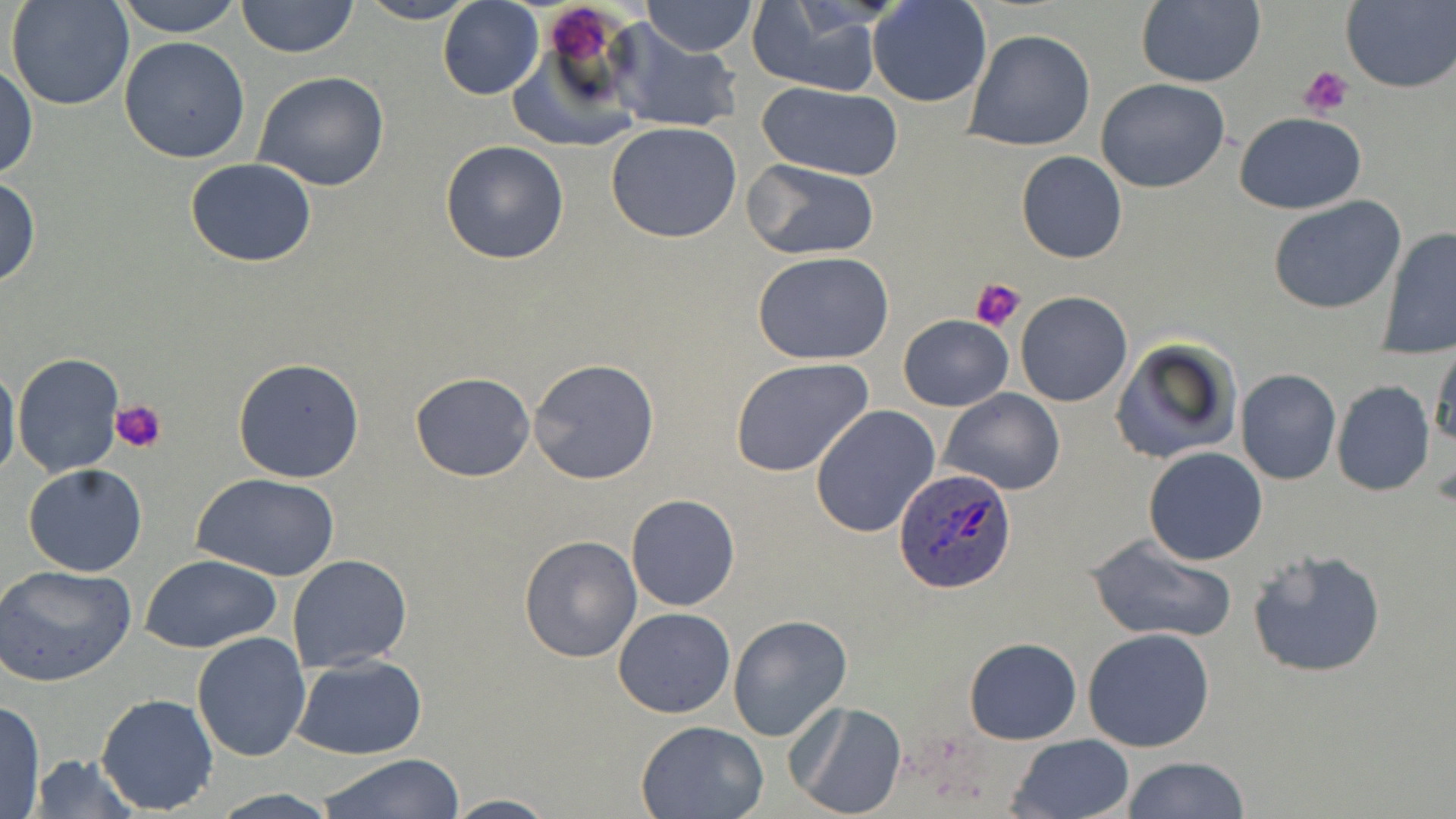
Approximate bounding boxes as named x1/y1/x2/y2 corners in pixels. Platelet locations: (x1=549, y1=8, x2=611, y2=62), (x1=1299, y1=65, x2=1352, y2=118), (x1=972, y1=277, x2=1024, y2=333), (x1=110, y1=398, x2=168, y2=454). Uninfected red blood cell locations: (x1=5, y1=0, x2=134, y2=111), (x1=114, y1=0, x2=244, y2=36), (x1=235, y1=0, x2=359, y2=60), (x1=639, y1=0, x2=758, y2=57), (x1=355, y1=1, x2=479, y2=24), (x1=437, y1=1, x2=544, y2=100), (x1=867, y1=1, x2=993, y2=107), (x1=1133, y1=1, x2=1267, y2=88), (x1=1341, y1=1, x2=1456, y2=93), (x1=743, y1=6, x2=890, y2=95), (x1=608, y1=24, x2=744, y2=134), (x1=506, y1=28, x2=643, y2=151), (x1=964, y1=28, x2=1096, y2=151), (x1=119, y1=37, x2=251, y2=163), (x1=0, y1=64, x2=37, y2=180), (x1=252, y1=71, x2=390, y2=192), (x1=1094, y1=77, x2=1230, y2=194), (x1=756, y1=82, x2=904, y2=182), (x1=1234, y1=112, x2=1367, y2=214), (x1=605, y1=122, x2=743, y2=243), (x1=439, y1=139, x2=570, y2=264), (x1=1016, y1=150, x2=1127, y2=264), (x1=185, y1=158, x2=317, y2=268), (x1=744, y1=160, x2=880, y2=259), (x1=0, y1=176, x2=41, y2=289), (x1=1267, y1=194, x2=1406, y2=315), (x1=1379, y1=229, x2=1456, y2=356), (x1=752, y1=252, x2=896, y2=364), (x1=1014, y1=292, x2=1134, y2=407), (x1=898, y1=315, x2=1013, y2=410), (x1=1109, y1=338, x2=1242, y2=465), (x1=1431, y1=342, x2=1456, y2=453), (x1=12, y1=352, x2=124, y2=478), (x1=729, y1=356, x2=878, y2=480), (x1=232, y1=357, x2=365, y2=483), (x1=528, y1=357, x2=660, y2=484), (x1=0, y1=362, x2=20, y2=488), (x1=1235, y1=369, x2=1341, y2=485), (x1=409, y1=371, x2=535, y2=482), (x1=1331, y1=380, x2=1435, y2=497), (x1=939, y1=388, x2=1065, y2=495), (x1=810, y1=406, x2=941, y2=540), (x1=1143, y1=447, x2=1269, y2=566), (x1=23, y1=464, x2=148, y2=577), (x1=195, y1=473, x2=339, y2=581), (x1=626, y1=493, x2=741, y2=612), (x1=1083, y1=532, x2=1236, y2=643), (x1=517, y1=533, x2=643, y2=663), (x1=1247, y1=548, x2=1387, y2=680), (x1=141, y1=555, x2=283, y2=652), (x1=287, y1=555, x2=413, y2=674), (x1=0, y1=564, x2=135, y2=687), (x1=613, y1=607, x2=735, y2=718), (x1=728, y1=615, x2=852, y2=741), (x1=1084, y1=627, x2=1216, y2=752), (x1=190, y1=631, x2=311, y2=761), (x1=964, y1=637, x2=1082, y2=745), (x1=291, y1=655, x2=427, y2=759), (x1=95, y1=693, x2=219, y2=813), (x1=0, y1=700, x2=46, y2=818), (x1=787, y1=700, x2=908, y2=819), (x1=636, y1=719, x2=771, y2=818), (x1=1009, y1=734, x2=1136, y2=819), (x1=318, y1=753, x2=466, y2=818), (x1=28, y1=754, x2=141, y2=818), (x1=1122, y1=756, x2=1250, y2=818), (x1=208, y1=789, x2=344, y2=819), (x1=443, y1=794, x2=559, y2=819). Plasmodium ovale-infected red blood cell locations: (x1=893, y1=469, x2=1018, y2=593). Slide-level diagnosis: Plasmodium ovale. Image is 1456×819 pixels. Optical microscopy. Thin blood smear. May-Grünwald-Giemsa-stained preparation. 1000x magnification. One field of a larger specimen.